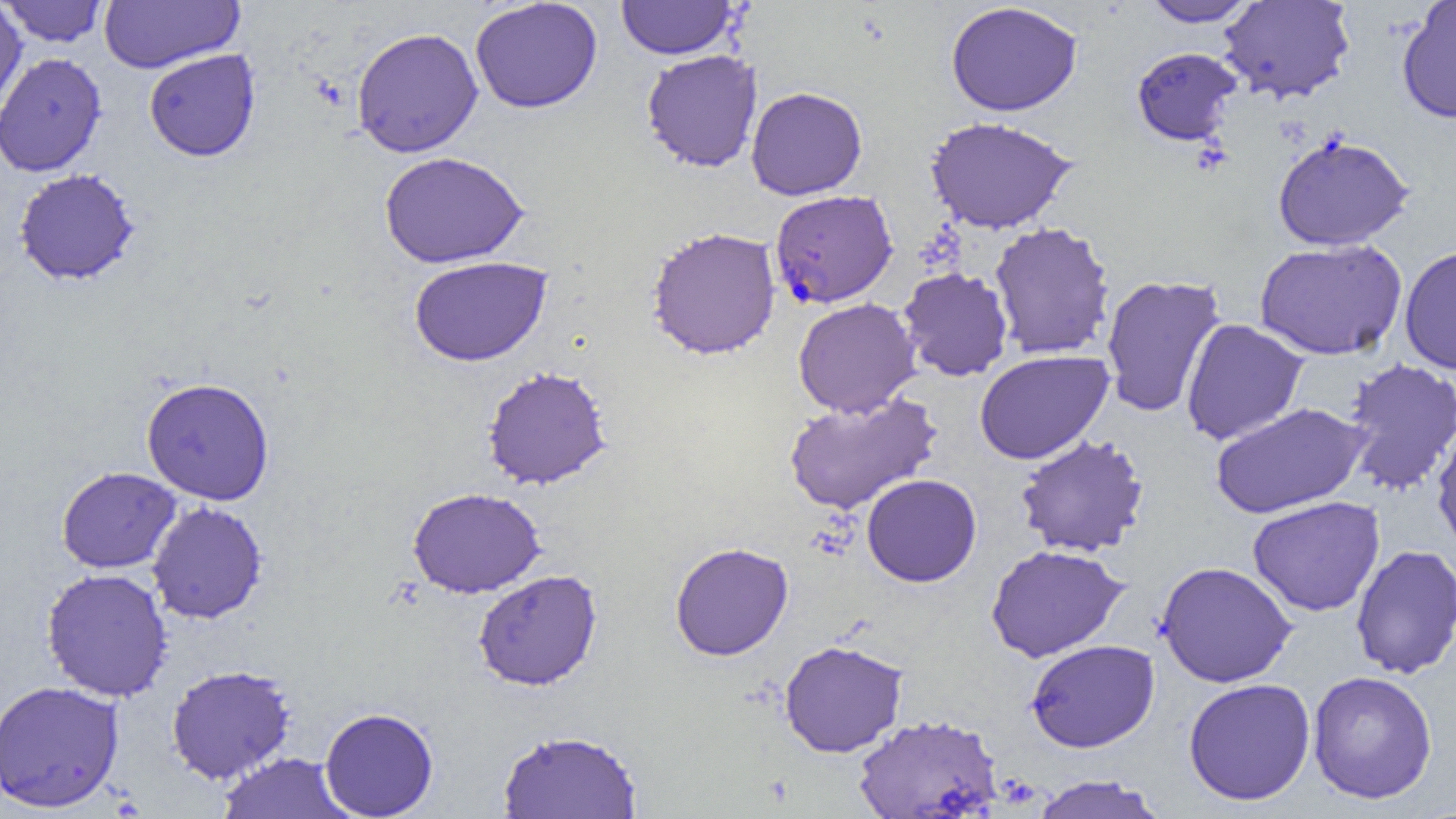

Summary:
  - Coordinate format: approximate bounding boxes as (x1, y1, x2, y2) in pixels
  - Plasmodium falciparum-infected red blood cell locations: (769, 189, 898, 309)
  - Uninfected red blood cell locations: (99, 0, 244, 73), (617, 0, 737, 59), (1218, 0, 1355, 103), (2, 1, 108, 47), (469, 1, 603, 114), (1141, 1, 1259, 27), (945, 2, 1083, 117), (1396, 2, 1456, 123), (0, 6, 29, 122), (351, 27, 484, 159), (1131, 46, 1243, 147), (144, 49, 261, 162), (641, 49, 763, 173), (0, 52, 107, 177), (746, 86, 867, 200), (925, 116, 1077, 234), (1272, 132, 1414, 251), (379, 151, 529, 268), (14, 169, 140, 286), (989, 222, 1116, 359), (646, 226, 781, 360), (1254, 239, 1408, 361), (1399, 245, 1456, 375), (408, 256, 552, 366), (898, 267, 1013, 381), (1100, 274, 1227, 418), (793, 297, 922, 418), (1180, 318, 1309, 445), (974, 349, 1114, 465), (1340, 358, 1456, 496), (482, 366, 612, 490), (141, 376, 275, 505), (784, 391, 943, 515), (1209, 402, 1370, 519), (1432, 423, 1456, 556), (1015, 434, 1150, 558), (56, 466, 182, 573), (861, 474, 982, 587), (407, 487, 545, 598), (1247, 496, 1385, 617), (147, 501, 268, 624), (669, 542, 794, 661), (986, 544, 1129, 663), (1350, 544, 1456, 679), (1155, 561, 1298, 687), (41, 568, 174, 702), (473, 570, 602, 691), (779, 639, 909, 757), (1025, 639, 1160, 752), (165, 665, 296, 784), (1307, 670, 1438, 804), (1183, 678, 1316, 806), (0, 681, 125, 813), (320, 707, 439, 818), (854, 714, 1003, 819), (497, 728, 642, 819), (217, 752, 355, 818), (1031, 774, 1166, 819)
  - Slide-level diagnosis: Plasmodium falciparum
  - Modality: optical microscopy
  - Magnification: 1000x
  - Field of view: one of a larger specimen
  - Preparation: thin blood smear
  - Image size: 1456×819 pixels